Classify this cell by malaria status.
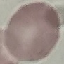

Uninfected.

Giemsa-stained preparation. Thin blood smear. Cell patch, automatically extracted from a larger field of view and resized to 64 × 64 pixels. Photographed with a smartphone camera at the microscope eyepiece.